Describe the morphology of the red blood cells.
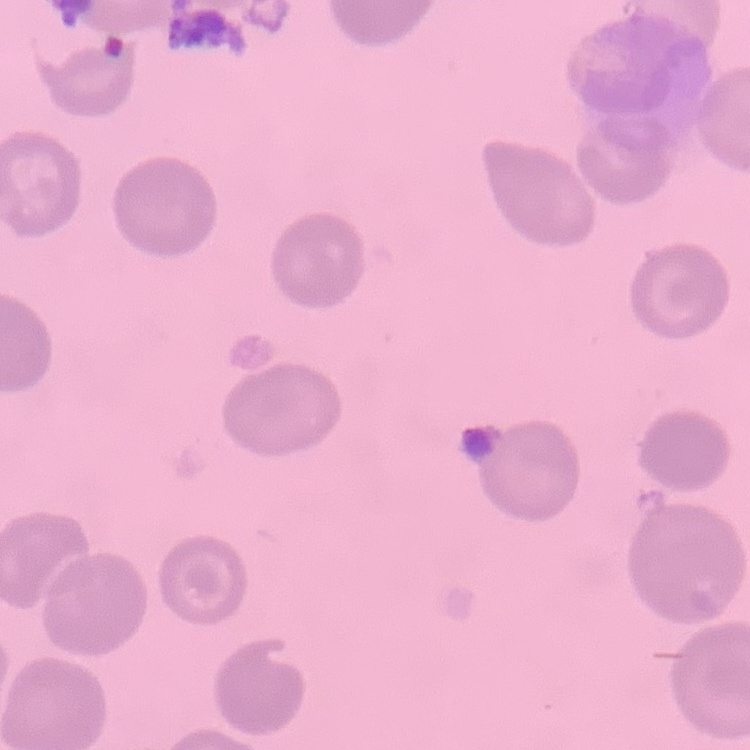

No rouleaux formation.

stain = Field's or Giemsa
image type = one tile cut from a larger photomicrograph
preparation = thin blood smear